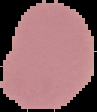
Summary:
  - Preparation: thin blood smear
  - Malaria status: uninfected
  - Image type: cell region segmented out of the field of view; surrounding area masked to black
  - Image size: 97×112 pixels